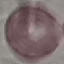

Summary:
  - Malaria status: uninfected
  - Preparation: thin smear
  - Capture: smartphone through the microscope eyepiece
  - Stain: Giemsa
  - Image type: automatically extracted cell patch, resized to 64 × 64 pixels